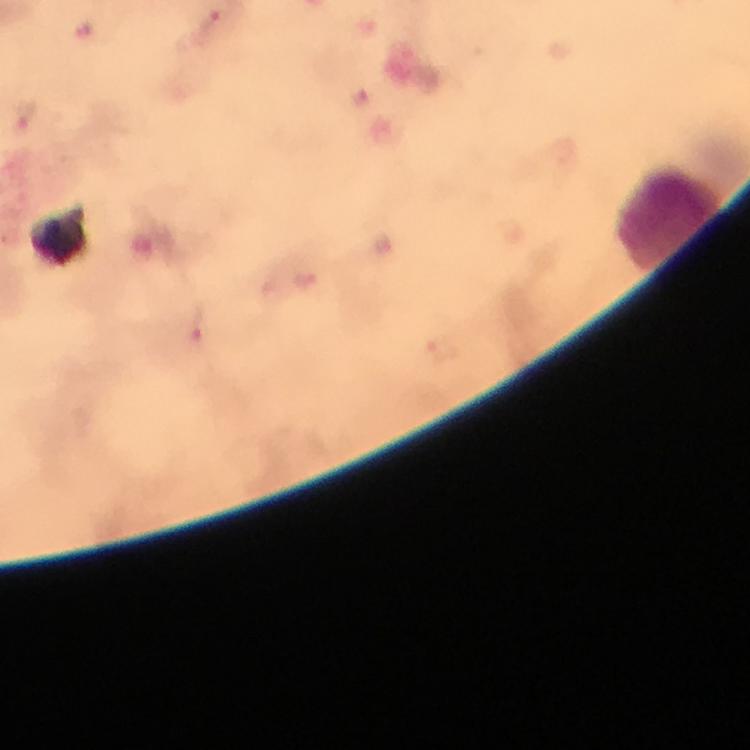

Approximate centers as {x, y} in pixels. Leukocyte locations: {667, 217}. Plasmodium parasite locations: {216, 26}, {357, 96}, {25, 117}, {195, 323}. Giemsa stain. At 100x magnification. Photographed through the microscope with a smartphone camera. Image is 750×750 pixels. Immersion oil applied. From a malaria diagnostic workup. A crop from one field of view. Thick smear.